Outline each blood parasite and name the species.
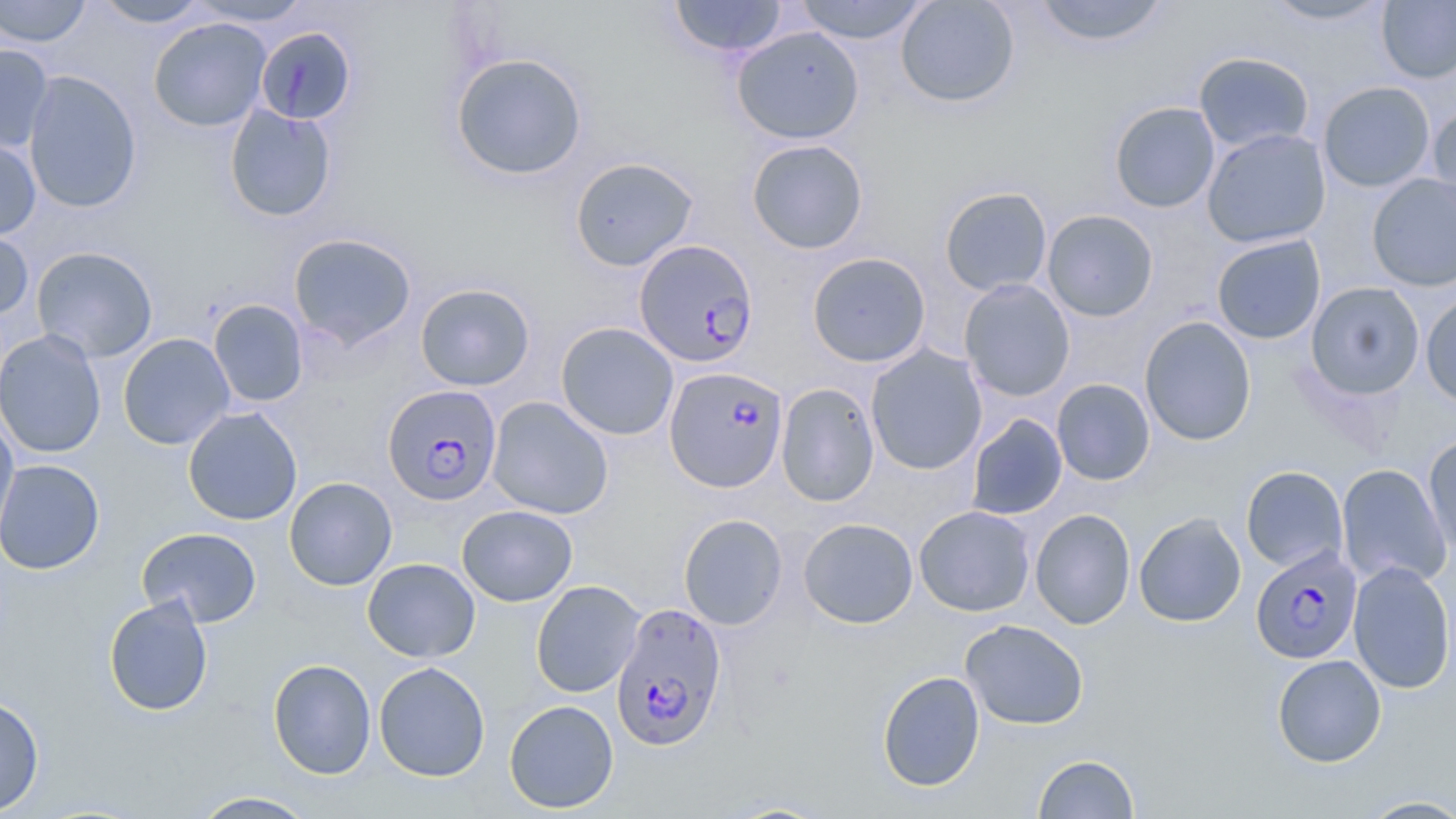

Approximate bounding boxes as (x1, y1, x2, y2) in pixels.
Plasmodium falciparum-infected red blood cells: (634, 239, 758, 368), (665, 366, 788, 493), (382, 384, 503, 506), (1251, 545, 1363, 664), (611, 601, 728, 751).
No Plasmodium ovale, Plasmodium malariae, Plasmodium vivax, Babesia divergens, or Trypanosoma brucei observed.

Uninfected red blood cell locations: (0, 0, 92, 47), (91, 0, 213, 28), (187, 0, 313, 27), (669, 0, 788, 58), (793, 0, 931, 45), (895, 0, 1020, 108), (1030, 0, 1171, 47), (1261, 0, 1393, 26), (1377, 1, 1456, 84), (148, 17, 271, 132), (731, 26, 865, 144), (255, 27, 357, 126), (0, 43, 54, 153), (1194, 51, 1315, 154), (450, 52, 588, 181), (23, 70, 142, 213), (1318, 81, 1435, 192), (1108, 101, 1221, 213), (1427, 101, 1456, 225), (224, 104, 337, 222), (1109, 113, 1329, 225), (1201, 128, 1331, 248), (0, 136, 41, 241), (746, 139, 869, 254), (570, 157, 699, 271), (1367, 173, 1456, 291), (939, 186, 1053, 297), (1042, 209, 1159, 322), (0, 219, 34, 322), (288, 232, 417, 350), (1211, 234, 1326, 345), (31, 246, 158, 362), (807, 252, 930, 368), (959, 278, 1075, 401), (1306, 282, 1424, 400), (415, 283, 535, 391), (1420, 292, 1456, 409), (208, 299, 309, 407), (1139, 316, 1256, 446), (556, 322, 679, 441), (0, 330, 106, 458), (118, 333, 235, 450), (866, 345, 987, 475), (1051, 378, 1155, 486), (776, 383, 880, 507), (487, 396, 614, 519), (183, 406, 303, 525), (0, 412, 19, 550), (966, 413, 1068, 520), (1422, 433, 1456, 557), (0, 460, 105, 574), (1336, 464, 1452, 590), (1241, 465, 1348, 572), (284, 477, 397, 590), (457, 505, 577, 606), (914, 505, 1035, 617), (1030, 508, 1136, 629), (1134, 512, 1246, 628), (678, 514, 787, 630), (798, 517, 918, 628), (136, 526, 262, 627), (362, 558, 480, 663), (1348, 561, 1456, 694), (530, 580, 645, 698), (104, 595, 214, 716), (960, 619, 1089, 730), (1271, 654, 1386, 767), (267, 659, 376, 779), (374, 661, 490, 782), (876, 671, 985, 792), (0, 694, 44, 816), (504, 700, 619, 813), (1033, 754, 1140, 818), (189, 791, 320, 818), (1357, 795, 1456, 818). Slide-level diagnosis: Plasmodium falciparum. Image is 1456×819 pixels. Thin blood film. May-Grünwald-Giemsa stain. Optical microscopy. One field of a larger specimen. Captured at 1000x magnification.